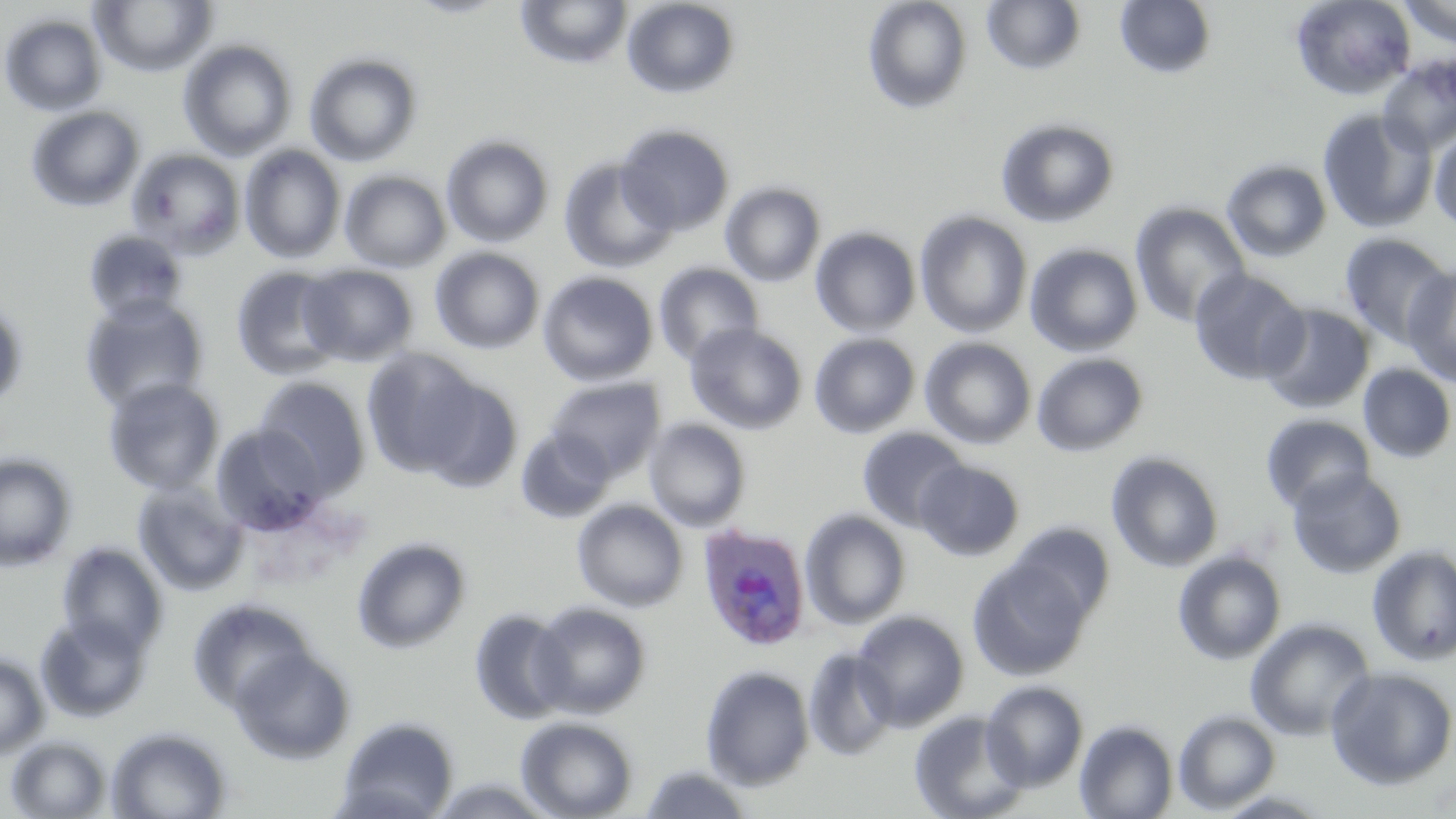

Approximate bounding boxes as (x1,y1)-(x2,y2) corner pairs in pixels. Plasmodium ovale-infected red blood cell locations: (696,523)-(812,651). Uninfected red blood cell locations: (89,0)-(218,77), (403,0)-(515,19), (515,0)-(633,69), (862,0)-(972,114), (981,0)-(1086,75), (1114,0)-(1217,79), (1290,0)-(1416,100), (1397,0)-(1456,48), (622,1)-(741,99), (0,13)-(108,116), (178,39)-(299,160), (304,51)-(424,167), (1377,55)-(1456,156), (26,105)-(145,212), (1317,106)-(1438,233), (995,117)-(1120,228), (615,123)-(735,236), (1430,130)-(1456,231), (441,134)-(554,247), (240,145)-(347,263), (126,149)-(245,258), (558,157)-(678,272), (1221,159)-(1333,262), (340,170)-(451,273), (720,181)-(826,287), (1130,202)-(1251,328), (915,211)-(1032,338), (810,226)-(922,337), (83,229)-(189,323), (1338,232)-(1454,349), (1024,243)-(1143,356), (430,247)-(545,355), (430,258)-(657,372), (653,262)-(764,365), (299,264)-(417,366), (1401,264)-(1456,387), (231,266)-(346,381), (1188,268)-(1309,386), (537,271)-(658,386), (79,294)-(209,415), (0,298)-(29,413), (1259,303)-(1375,414), (685,323)-(807,434), (809,333)-(920,439), (920,337)-(1037,449), (360,347)-(485,479), (1031,352)-(1149,457), (1357,363)-(1456,464), (414,372)-(524,493), (547,376)-(665,479), (103,377)-(225,496), (253,377)-(371,495), (1260,413)-(1376,514), (643,418)-(752,532), (210,423)-(328,535), (856,426)-(971,533), (515,429)-(616,523), (1106,451)-(1224,573), (0,452)-(77,571), (915,460)-(1024,561), (1286,468)-(1407,580), (132,480)-(248,596), (572,499)-(688,612), (800,509)-(912,630), (1006,520)-(1116,629), (351,536)-(472,655), (56,541)-(168,657), (1366,544)-(1456,666), (1355,546)-(1456,794), (1172,549)-(1287,666), (968,557)-(1092,681), (187,598)-(315,715), (529,602)-(651,718), (469,608)-(572,725), (850,609)-(969,731), (35,614)-(151,723), (1245,617)-(1375,741), (229,646)-(355,764), (803,646)-(899,762), (0,652)-(49,759), (700,665)-(815,790), (1324,667)-(1456,790), (981,680)-(1089,791), (908,709)-(1030,819), (1173,709)-(1281,814), (334,715)-(460,819), (515,716)-(638,818), (1074,719)-(1179,819), (106,726)-(232,819), (5,735)-(112,818), (639,763)-(755,818), (427,774)-(558,818). Slide-level diagnosis: Plasmodium ovale. Thin blood film. Light microscopy. May-Grünwald-Giemsa-stained preparation. Single field of view. Captured at 1000x magnification. Image is 1456×819 pixels.